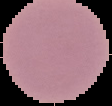

Summary:
  - Image type: cell region segmented out of the field of view; surrounding area masked to black
  - Result: no Plasmodium parasites detected
  - Preparation: thin blood film
  - Image size: 112×106 pixels